Assess the morphology of the red blood cells.
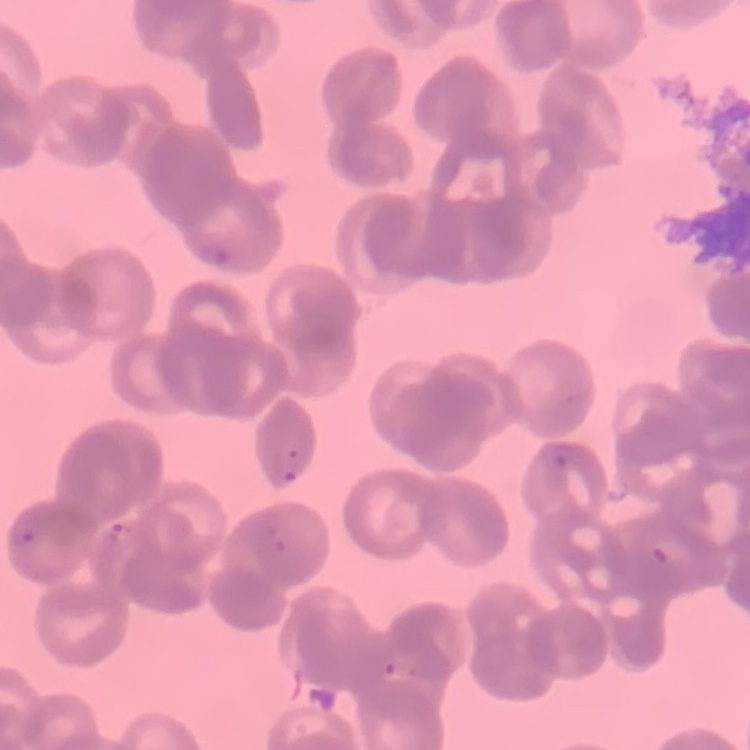

They show rouleaux formation.

Stained with either Field's or Giemsa. Thin blood film. Square crop of a larger photomicrograph.